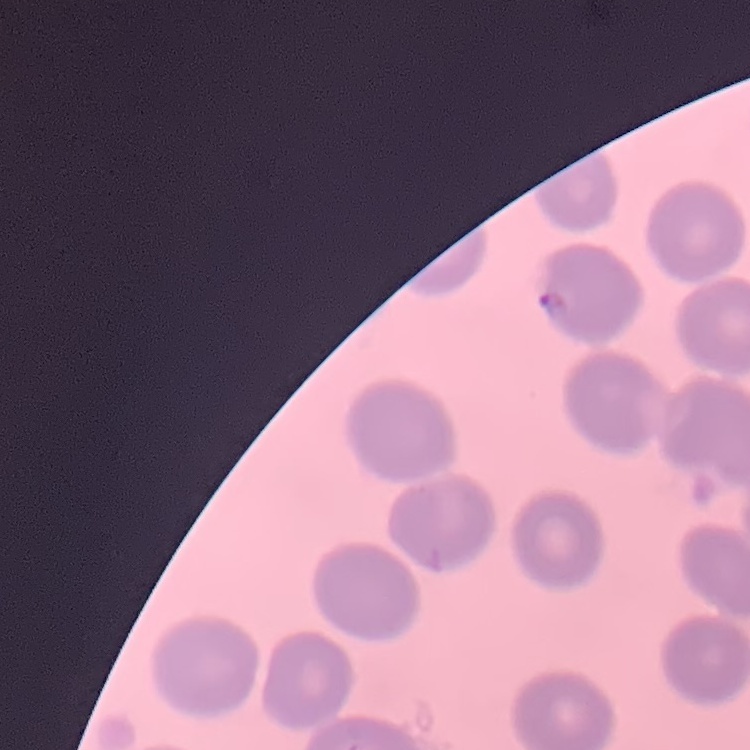 The erythrocytes show no rouleaux formation. Field's or Giemsa stain. Thin blood smear. Square crop of a larger photomicrograph.